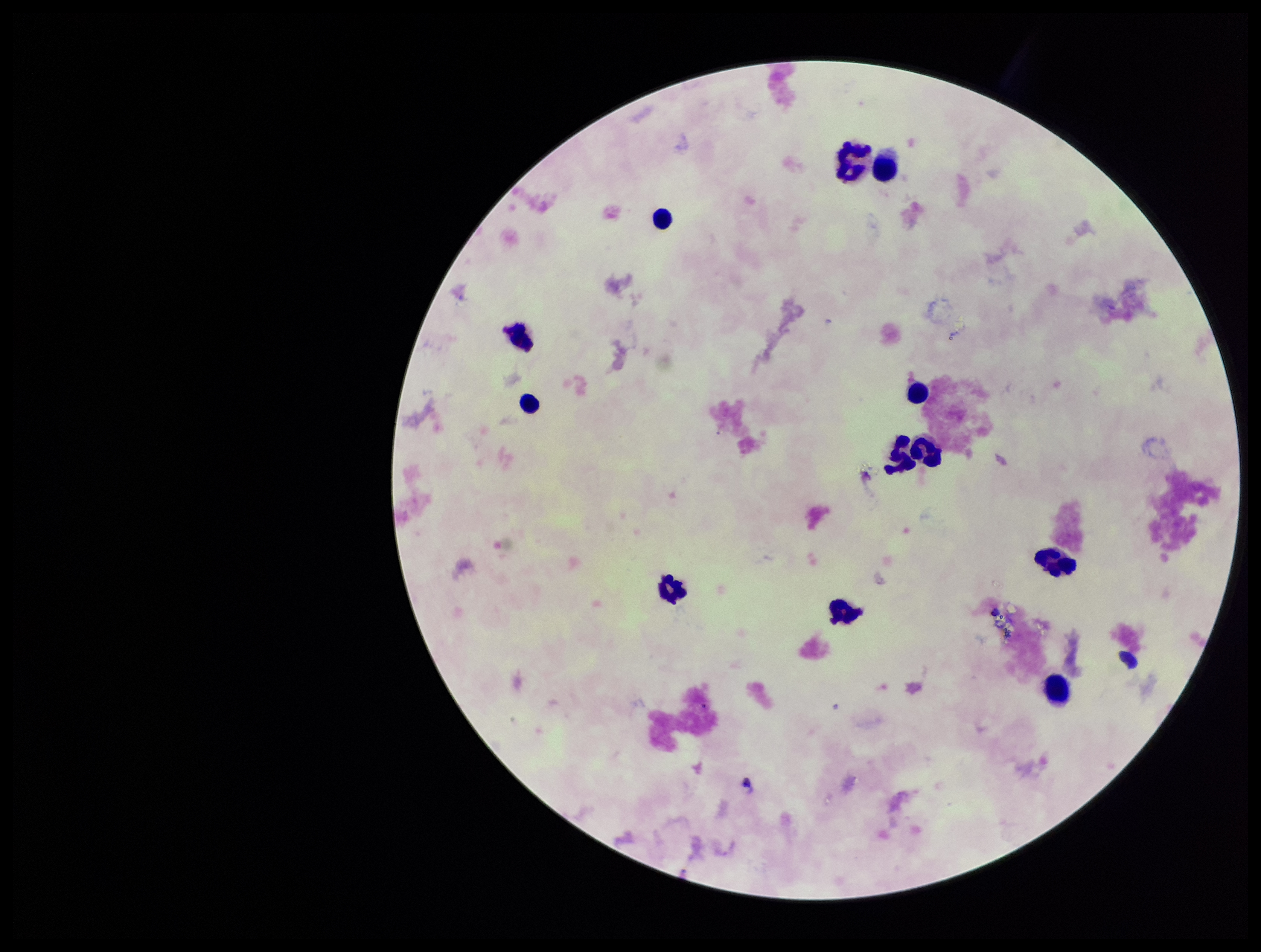
capture: smartphone photograph through the microscope eyepiece
patient_malaria_status: negative
preparation: thick blood smear
parasite_count: 0
image_size: 1261×952 pixels
plasmodium_parasites: none seen
stain: Giemsa
field_of_view: single
leukocyte_count: 12